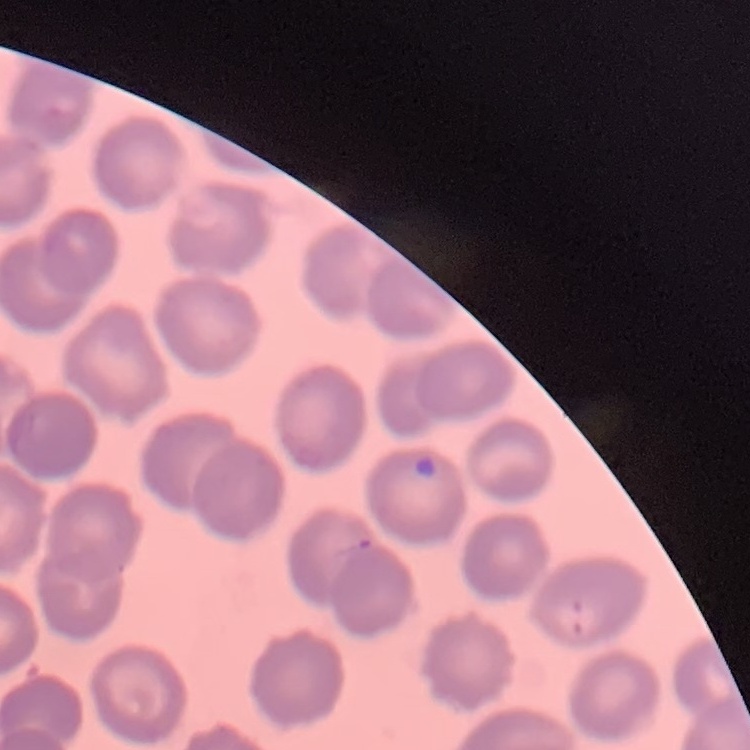
{
  "erythrocyte_morphology": "no rouleaux formation",
  "stain": "Field's or Giemsa",
  "preparation": "thin blood smear",
  "image_type": "one tile cut from a larger photomicrograph"
}